State which parasite is depicted.
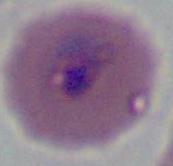

This is Plasmodium.

Micrograph. Captured at either 400x or 1000x magnification.